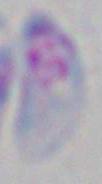
1000x magnification. Photomicrograph. Toxoplasma gondii is shown.